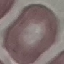 Malaria status: uninfected. Giemsa-stained preparation. Acquired by smartphone through the microscope eyepiece. Thin blood film. Cell patch, automatically extracted from a larger field of view and resized to 64 × 64 pixels.